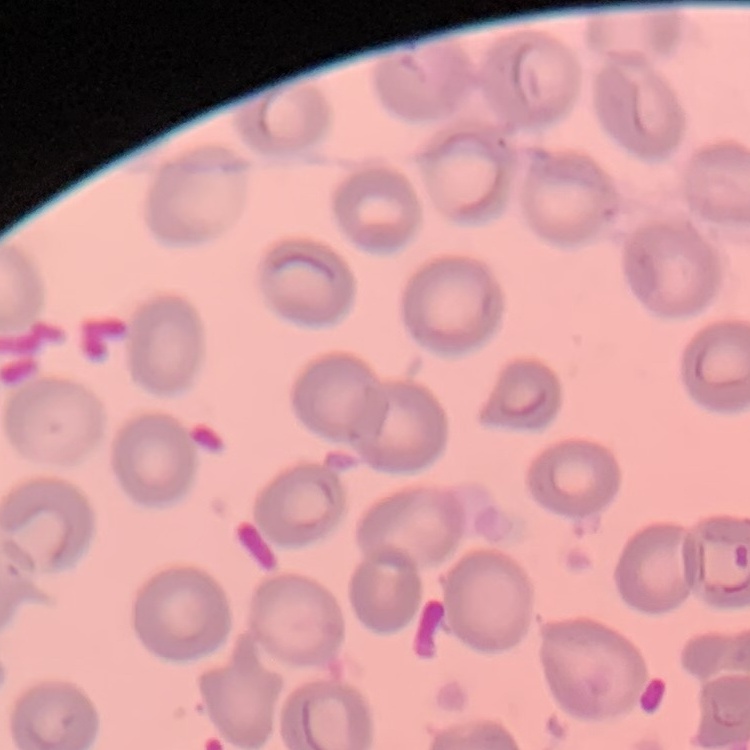
{
  "red_blood_cell_morphology": "no rouleaux formation",
  "preparation": "thin blood film",
  "image_type": "square crop of a larger photomicrograph",
  "stain": "Field's or Giemsa"
}